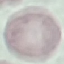

Malaria status: uninfected. Thin smear of blood. Automatically extracted cell patch, resized to 64 × 64 pixels. Giemsa-stained preparation. Acquired by smartphone through the microscope eyepiece.